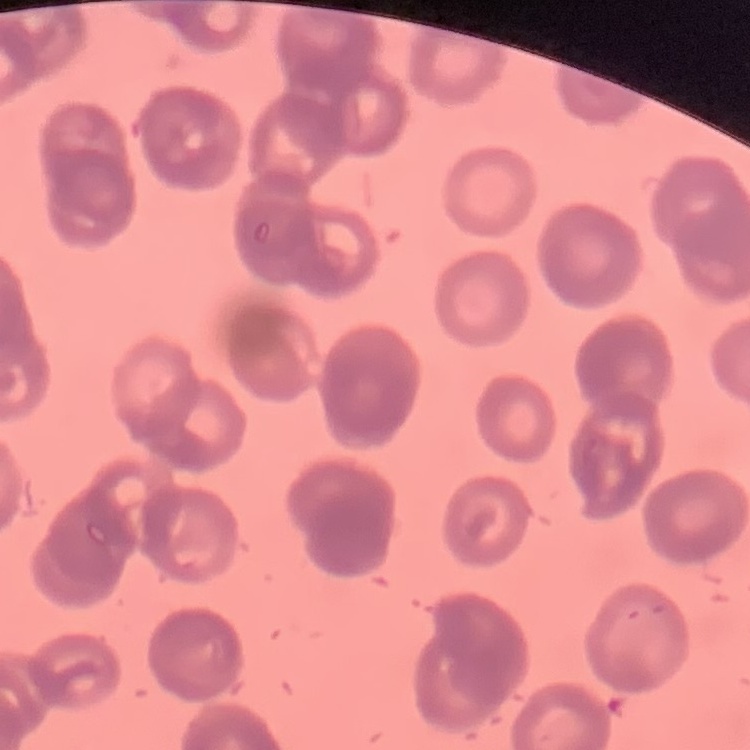

red blood cell morphology = rouleaux formation
preparation = thin blood film
image type = one tile cut from a larger photomicrograph
stain = Field's or Giemsa